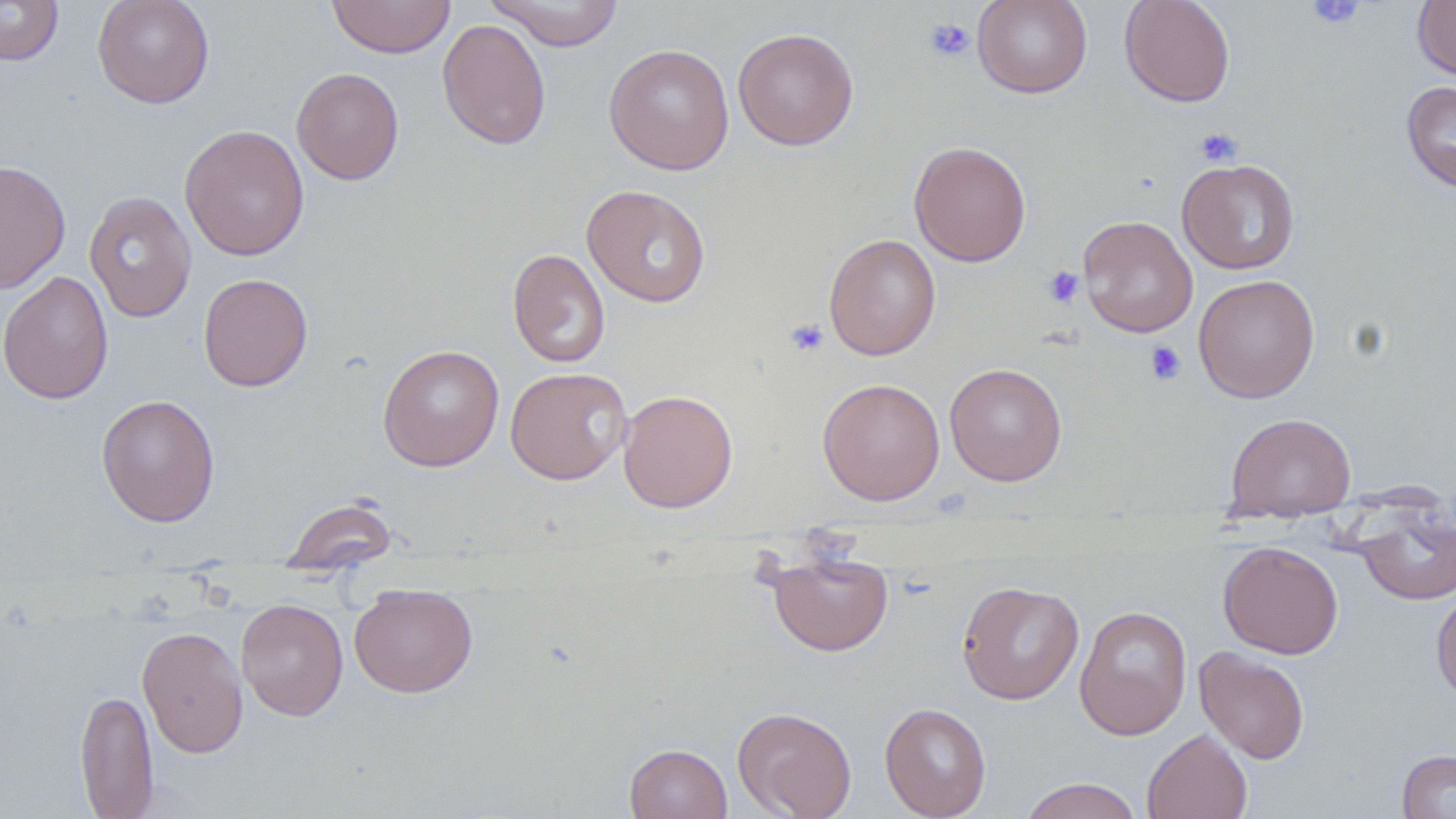
slide-level diagnosis = no evidence of blood parasites
stain = May-Grünwald-Giemsa
field of view = one of a larger specimen
platelet locations = approximate bounding boxes as (x1, y1, x2, y2) in pixels: (1305, 0, 1365, 30), (924, 18, 975, 61), (1194, 127, 1242, 168), (1043, 266, 1084, 308), (784, 318, 829, 357), (1144, 340, 1186, 385)
modality = light microscopy
uninfected red blood cell locations = approximate bounding boxes as (x1, y1, x2, y2) in pixels: (0, 0, 64, 67), (92, 0, 215, 108), (326, 0, 456, 58), (484, 0, 624, 51), (972, 0, 1092, 98), (1119, 0, 1236, 107), (1412, 0, 1456, 80), (437, 18, 552, 150), (732, 28, 859, 150), (604, 43, 735, 175), (291, 67, 404, 184), (1401, 81, 1456, 194), (179, 123, 309, 262), (909, 141, 1032, 267), (1177, 158, 1300, 275), (0, 159, 71, 294), (581, 184, 711, 307), (84, 191, 197, 323), (1078, 215, 1198, 337), (823, 233, 941, 361), (508, 248, 610, 368), (0, 270, 114, 405), (198, 273, 313, 391), (1193, 274, 1320, 403), (377, 344, 504, 471), (944, 363, 1067, 486), (504, 367, 633, 485), (817, 377, 946, 505), (618, 389, 738, 513), (96, 393, 220, 527), (1224, 412, 1357, 520), (279, 495, 399, 573), (1356, 508, 1456, 605), (1217, 541, 1344, 659), (767, 550, 893, 656), (956, 581, 1084, 705), (349, 583, 478, 698), (1431, 590, 1456, 708), (236, 599, 348, 721), (1074, 604, 1193, 741), (136, 625, 249, 758), (1194, 647, 1310, 764), (75, 688, 159, 817), (879, 702, 991, 819), (732, 706, 858, 819), (1142, 728, 1252, 819), (624, 743, 732, 819), (1397, 749, 1456, 818), (1017, 777, 1144, 819)
magnification = 1000x
image size = 1456×819 pixels
preparation = thin blood smear